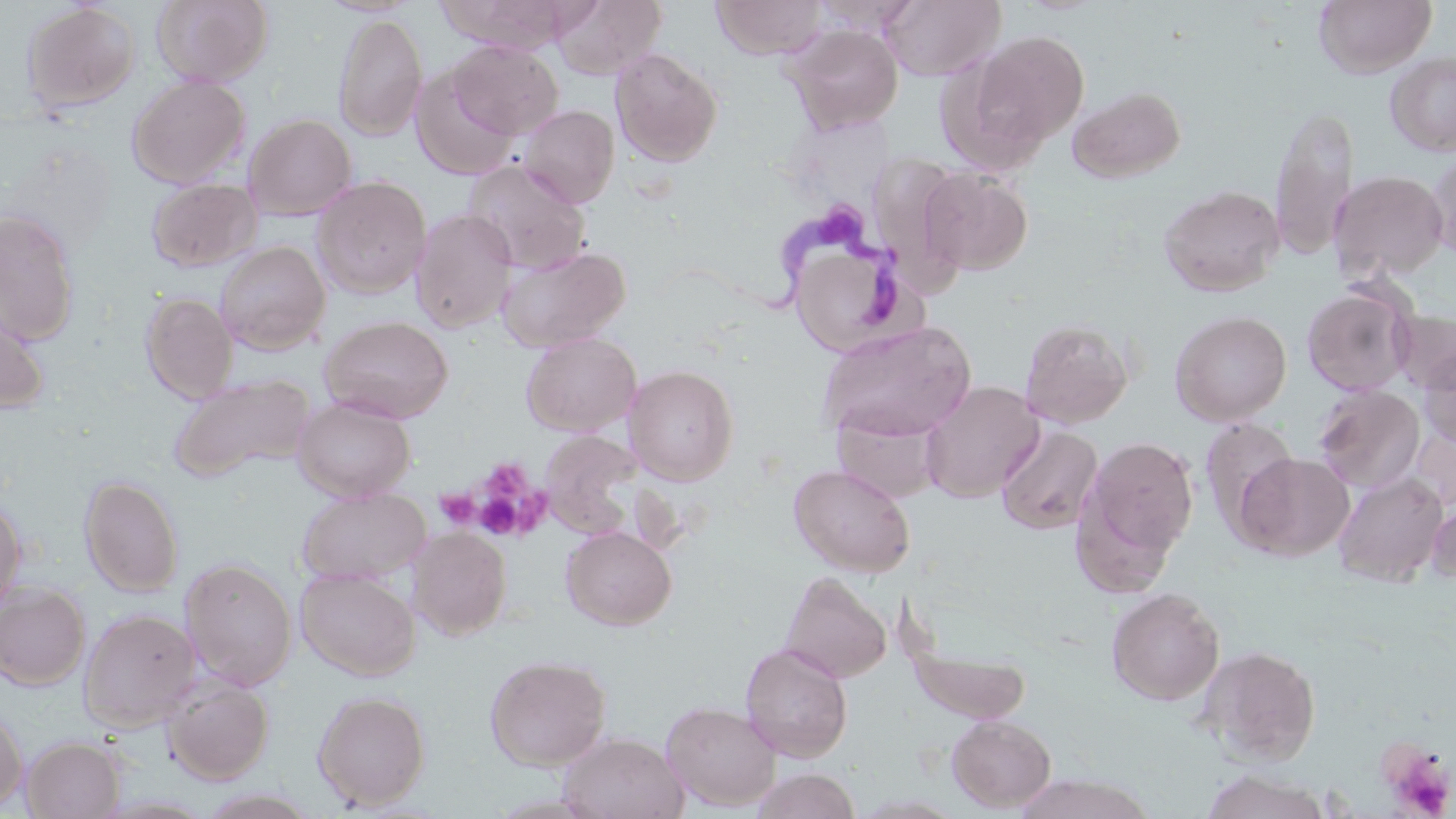

Summary:
  - Coordinate format: approximate bounding boxes as (x1, y1, x2, y2) in pixels
  - Uninfected red blood cell locations: (152, 0, 273, 87), (438, 0, 576, 54), (550, 0, 667, 80), (710, 0, 827, 59), (880, 0, 1004, 81), (1314, 0, 1435, 78), (21, 2, 140, 113), (333, 11, 427, 142), (783, 23, 903, 134), (963, 29, 1090, 157), (448, 40, 563, 139), (609, 46, 723, 166), (1385, 51, 1456, 157), (410, 67, 520, 181), (127, 75, 251, 189), (1067, 86, 1186, 183), (1269, 103, 1359, 262), (517, 104, 619, 208), (243, 113, 357, 220), (1, 141, 118, 256), (1424, 148, 1456, 261), (463, 160, 591, 274), (919, 167, 1033, 276), (1329, 170, 1448, 283), (312, 176, 431, 299), (147, 178, 262, 272), (1158, 184, 1284, 297), (410, 208, 517, 334), (0, 210, 80, 345), (215, 240, 330, 354), (790, 240, 909, 355), (497, 245, 631, 351), (1302, 282, 1417, 397), (140, 292, 238, 403), (0, 298, 50, 416), (1170, 309, 1292, 426), (1389, 309, 1456, 394), (319, 315, 453, 422), (1019, 317, 1135, 428), (816, 321, 976, 442), (521, 332, 641, 436), (1417, 348, 1456, 450), (624, 365, 740, 485), (167, 373, 317, 483), (920, 380, 1044, 502), (1313, 384, 1425, 493), (292, 396, 415, 502), (832, 411, 940, 504), (1198, 417, 1299, 539), (996, 424, 1103, 535), (541, 432, 643, 538), (1079, 435, 1199, 570), (1233, 451, 1355, 561), (788, 463, 915, 577), (1333, 471, 1448, 588), (79, 475, 184, 597), (297, 487, 429, 585), (0, 497, 26, 613), (1427, 501, 1456, 586), (409, 526, 512, 640), (560, 526, 676, 630), (180, 558, 298, 691), (296, 567, 420, 681), (780, 571, 891, 683), (0, 583, 90, 690), (1107, 588, 1225, 706), (79, 608, 200, 731), (740, 641, 853, 762), (1195, 645, 1321, 764), (909, 647, 1031, 724), (485, 654, 611, 771), (162, 676, 274, 784), (313, 690, 430, 810), (660, 701, 782, 811), (0, 704, 28, 811), (946, 715, 1056, 812), (557, 732, 688, 819), (21, 736, 124, 818), (749, 767, 862, 819), (1200, 770, 1331, 819), (1012, 774, 1153, 819)
  - Trypanosoma brucei locations: (757, 206, 913, 330)
  - Platelet locations: (477, 463, 547, 536), (434, 490, 479, 530), (1379, 741, 1455, 818)
  - Slide-level diagnosis: Trypanosoma brucei
  - Modality: light microscopy
  - Preparation: thin blood film
  - Magnification: 1000x
  - Field of view: one of a larger specimen
  - Image size: 1456×819 pixels
  - Stain: May-Grünwald-Giemsa